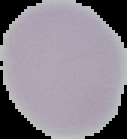

image size = 127×139 pixels
preparation = thin blood film
image type = cell region segmented out of the field of view; surrounding area masked to black
result = no malaria parasites detected